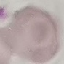
Summary:
  - Result: no malaria parasites seen
  - Preparation: thin blood film
  - Stain: Giemsa
  - Image type: automatically extracted cell patch, resized to 64 × 64 pixels
  - Capture: smartphone camera at the microscope eyepiece